Assess the morphology of the erythrocytes.
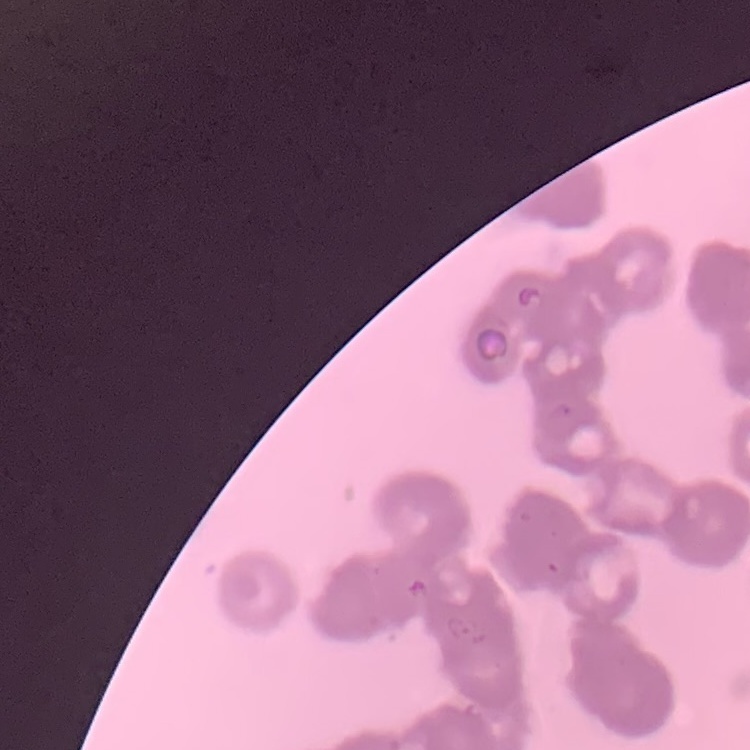

Rouleaux formation.

preparation = thin blood smear
stain = Field's or Giemsa
image type = square crop of a larger photomicrograph